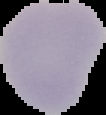
preparation = thin blood smear
image size = 106×115 pixels
image type = segmented cell region on a black background
result = no malaria parasites detected